Identify the parasite.
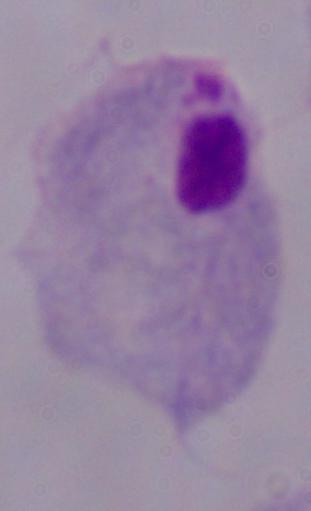

This is a trichomonad.

magnification = 1000x
modality = micrograph